Name the parasite shown.
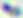
This is Toxoplasma gondii.

Summary:
  - Modality: photomicrograph
  - Magnification: 400x